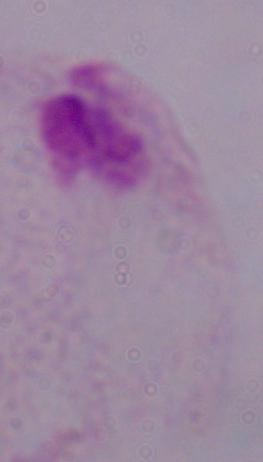

Summary:
  - Modality: photomicrograph
  - Identification: trichomonad
  - Magnification: 1000x